Assess this cell for malaria.
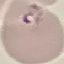

It is parasitized.

Summary:
  - Image type: cell patch, automatically extracted from a larger field of view and resized to 64 × 64 pixels
  - Preparation: thin blood smear
  - Capture: smartphone through the microscope eyepiece
  - Stain: Giemsa